Locate every P. falciparum parasite and give its life-cycle stage, and locate every leukocyte and any debris.
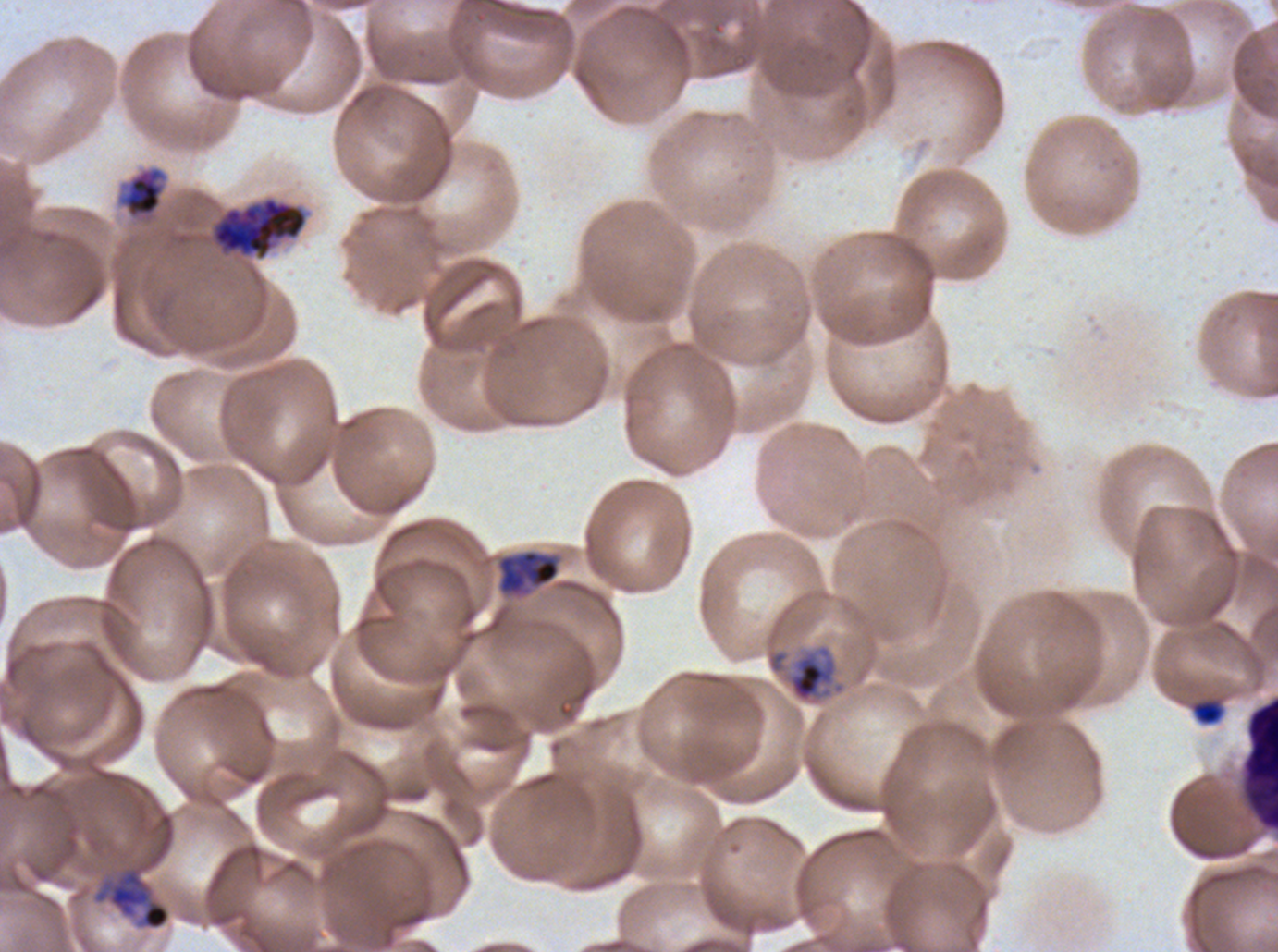
Approximate bounding boxes as {x1, y1, x2, y2} in pixels.
Mid trophozoites: {117, 165, 168, 220}, {497, 549, 560, 597}.
Late trophozoites: {785, 643, 846, 704}.
Late schizonts: {210, 196, 309, 262}, {94, 866, 171, 931}.
Leukocytes: {1240, 694, 1277, 833}.
Debris: {1192, 700, 1223, 725}.
No rings, late-ring/early-trophozoite forms, early schizonts, segmenters, or gametocytes observed.

Thin blood film. P. falciparum cultured ex vivo for 24 to 48 hours, from a patient in The Gambia. Image is 1278×952 pixels. One sub-image of a larger composite. Life-cycle stages observed: mid trophozoite, late trophozoite, late schizont. Giemsa-stained preparation.